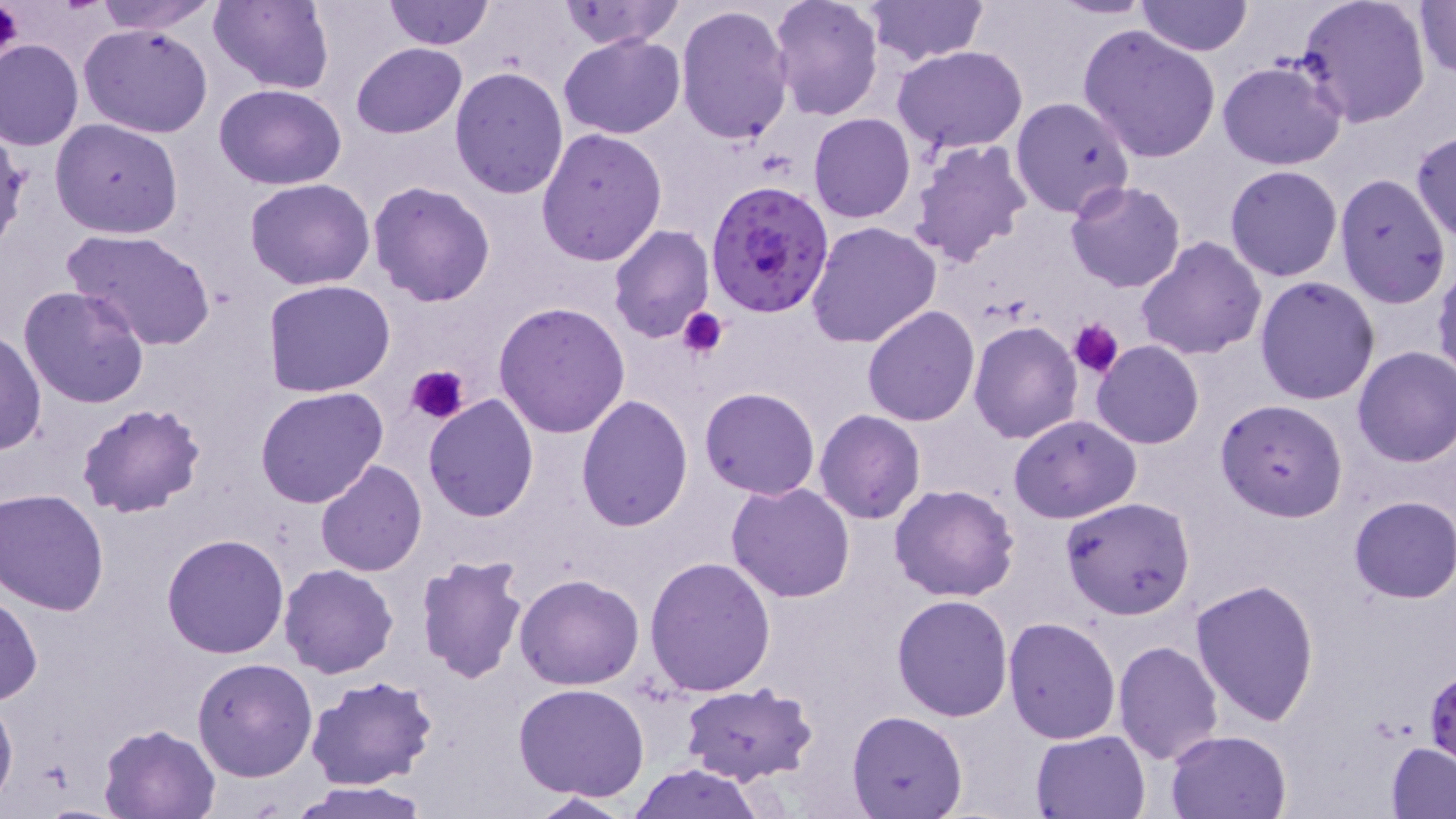
Summary:
  - Coordinate format: approximate bounding boxes as named x1/y1/x2/y2 corners in pixels
  - Plasmodium falciparum-infected red blood cell locations: (x1=705, y1=181, x2=835, y2=319)
  - Platelet locations: (x1=0, y1=0, x2=23, y2=67), (x1=676, y1=306, x2=728, y2=361), (x1=1069, y1=318, x2=1124, y2=379), (x1=406, y1=363, x2=469, y2=427)
  - Uninfected red blood cell locations: (x1=91, y1=0, x2=221, y2=33), (x1=210, y1=0, x2=333, y2=93), (x1=383, y1=0, x2=493, y2=49), (x1=771, y1=0, x2=884, y2=120), (x1=863, y1=0, x2=985, y2=65), (x1=1049, y1=0, x2=1156, y2=19), (x1=1134, y1=0, x2=1254, y2=56), (x1=1295, y1=0, x2=1433, y2=129), (x1=556, y1=1, x2=685, y2=50), (x1=1413, y1=1, x2=1456, y2=79), (x1=675, y1=3, x2=794, y2=145), (x1=868, y1=3, x2=1014, y2=113), (x1=80, y1=23, x2=214, y2=139), (x1=1077, y1=24, x2=1223, y2=161), (x1=559, y1=32, x2=687, y2=140), (x1=0, y1=40, x2=84, y2=151), (x1=351, y1=42, x2=467, y2=138), (x1=892, y1=46, x2=1029, y2=153), (x1=1216, y1=59, x2=1348, y2=169), (x1=448, y1=64, x2=570, y2=200), (x1=213, y1=83, x2=347, y2=190), (x1=1011, y1=96, x2=1135, y2=218), (x1=807, y1=113, x2=917, y2=223), (x1=49, y1=119, x2=184, y2=239), (x1=536, y1=127, x2=668, y2=267), (x1=1410, y1=129, x2=1456, y2=244), (x1=906, y1=139, x2=1032, y2=271), (x1=1224, y1=164, x2=1343, y2=282), (x1=1332, y1=174, x2=1451, y2=307), (x1=245, y1=178, x2=376, y2=290), (x1=368, y1=180, x2=496, y2=305), (x1=1064, y1=180, x2=1186, y2=293), (x1=805, y1=221, x2=942, y2=349), (x1=608, y1=226, x2=714, y2=344), (x1=64, y1=229, x2=218, y2=351), (x1=1135, y1=236, x2=1268, y2=361), (x1=1432, y1=261, x2=1456, y2=387), (x1=1255, y1=276, x2=1381, y2=406), (x1=262, y1=278, x2=396, y2=397), (x1=18, y1=285, x2=150, y2=408), (x1=494, y1=300, x2=631, y2=437), (x1=861, y1=306, x2=979, y2=426), (x1=968, y1=319, x2=1082, y2=442), (x1=0, y1=332, x2=46, y2=455), (x1=1091, y1=341, x2=1204, y2=449), (x1=1352, y1=347, x2=1456, y2=467), (x1=255, y1=387, x2=388, y2=508), (x1=699, y1=387, x2=820, y2=498), (x1=422, y1=394, x2=540, y2=521), (x1=576, y1=396, x2=693, y2=531), (x1=1215, y1=399, x2=1349, y2=522), (x1=75, y1=401, x2=206, y2=519), (x1=814, y1=411, x2=926, y2=525), (x1=1010, y1=414, x2=1141, y2=524), (x1=315, y1=460, x2=427, y2=577), (x1=726, y1=482, x2=857, y2=603), (x1=888, y1=484, x2=1020, y2=602), (x1=0, y1=490, x2=109, y2=615), (x1=1061, y1=496, x2=1195, y2=620), (x1=1348, y1=496, x2=1455, y2=603), (x1=162, y1=534, x2=290, y2=659), (x1=415, y1=552, x2=530, y2=685), (x1=644, y1=556, x2=777, y2=697), (x1=280, y1=563, x2=398, y2=678), (x1=515, y1=572, x2=645, y2=690), (x1=1192, y1=579, x2=1321, y2=727), (x1=0, y1=589, x2=41, y2=706), (x1=891, y1=593, x2=1014, y2=721), (x1=1004, y1=616, x2=1120, y2=742), (x1=1113, y1=640, x2=1224, y2=765), (x1=191, y1=657, x2=318, y2=781), (x1=305, y1=675, x2=439, y2=788), (x1=513, y1=682, x2=653, y2=801), (x1=678, y1=683, x2=819, y2=786), (x1=0, y1=691, x2=18, y2=809), (x1=846, y1=711, x2=967, y2=818), (x1=97, y1=722, x2=222, y2=818), (x1=1165, y1=728, x2=1292, y2=818), (x1=1031, y1=730, x2=1149, y2=819), (x1=1386, y1=741, x2=1456, y2=817), (x1=628, y1=764, x2=767, y2=819), (x1=284, y1=780, x2=429, y2=818), (x1=520, y1=792, x2=638, y2=818)
  - Slide-level diagnosis: Plasmodium falciparum
  - Stain: May-Grünwald-Giemsa
  - Preparation: thin blood film
  - Image size: 1456×819 pixels
  - Field of view: one of a larger specimen
  - Modality: light microscopy
  - Magnification: 1000x